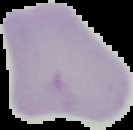

Summary:
  - Image type: segmented cell region on a black background
  - Image size: 133×130 pixels
  - Result: negative for Plasmodium parasites
  - Preparation: thin blood smear